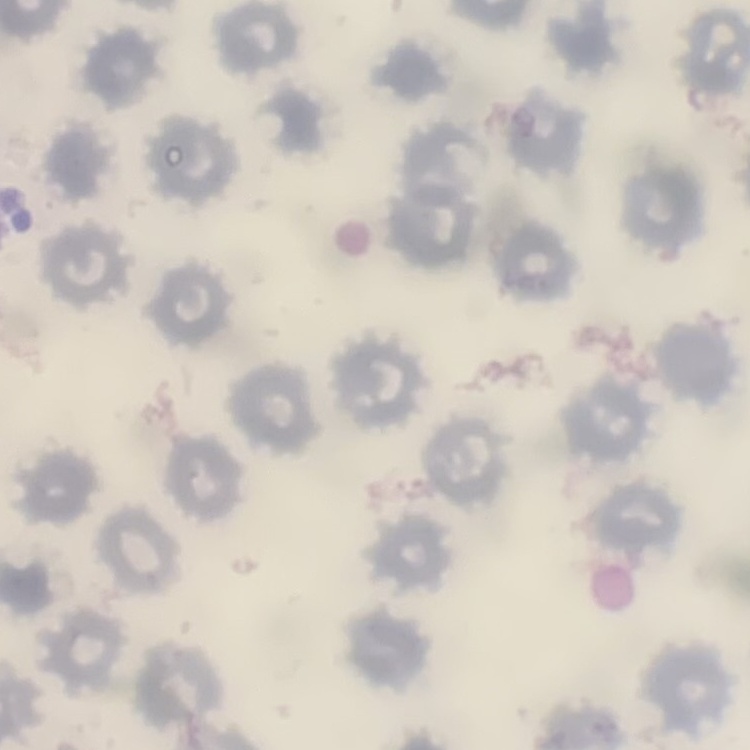
Summary:
  - Erythrocyte morphology: no rouleaux formation
  - Preparation: thin blood film
  - Stain: Field's or Giemsa
  - Image type: square crop of a larger photomicrograph